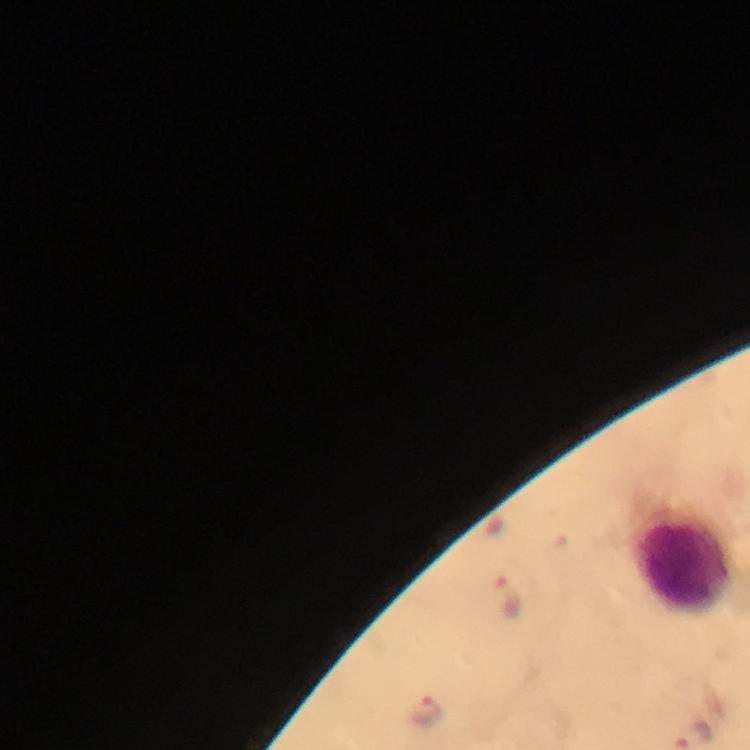

Approximate centers as {x, y} in pixels. Plasmodium parasite locations: {511, 598}, {427, 708}. Leukocyte locations: {684, 562}. From a malaria diagnostic workup. Smartphone photograph taken through a microscope. Thick blood smear. A crop from one field of view. Immersion oil was used. Image is 750×750 pixels. Giemsa-stained preparation. At 100x magnification.